Evaluate for Plasmodium parasites.
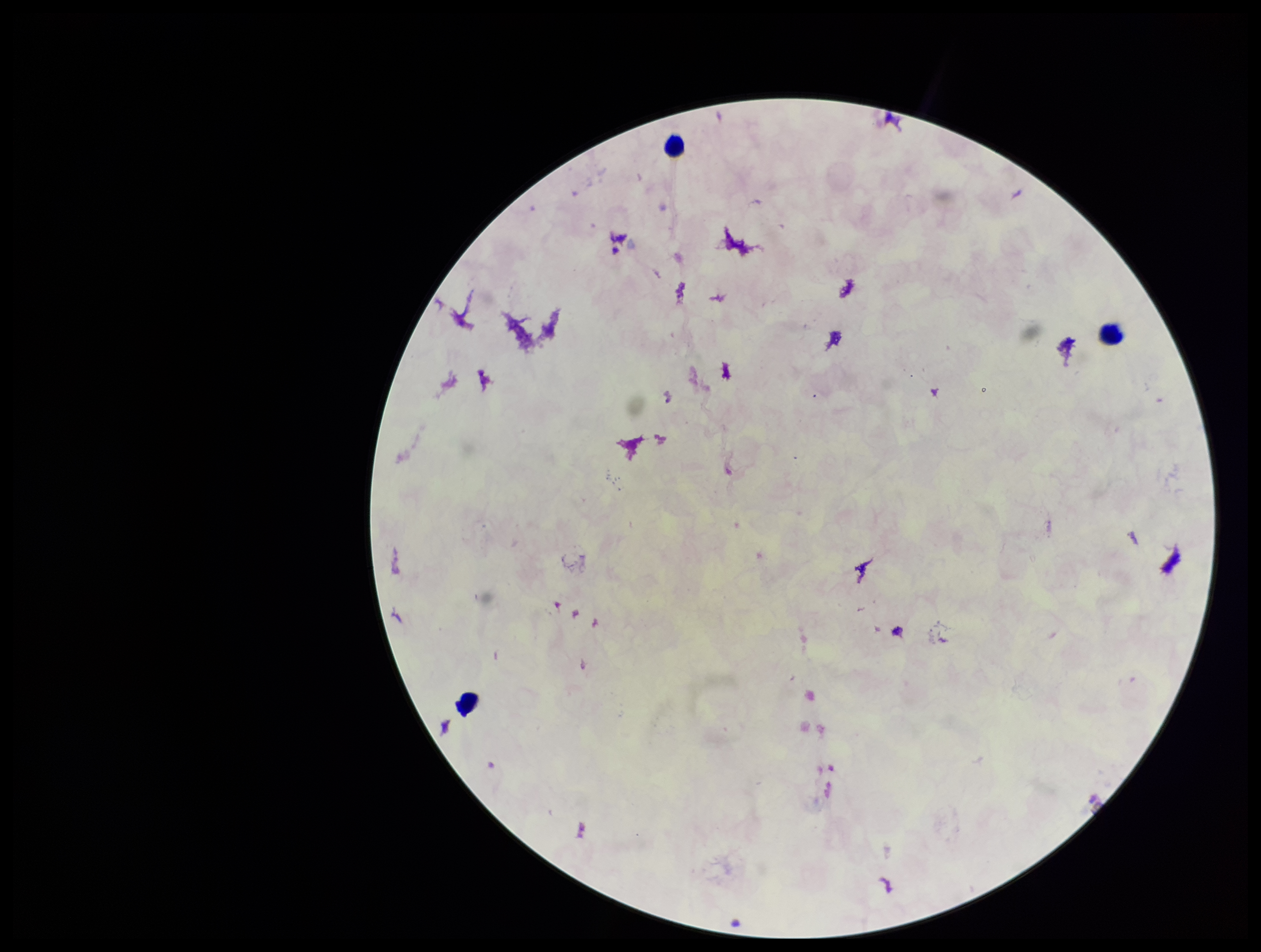
None identified.

Summary:
  - Image size: 1261×952 pixels
  - Stain: Giemsa
  - Parasite count: 0
  - Leukocyte count: 3
  - Patient malaria status: negative
  - Preparation: thick smear
  - Field of view: single
  - Capture: smartphone photograph through the microscope eyepiece